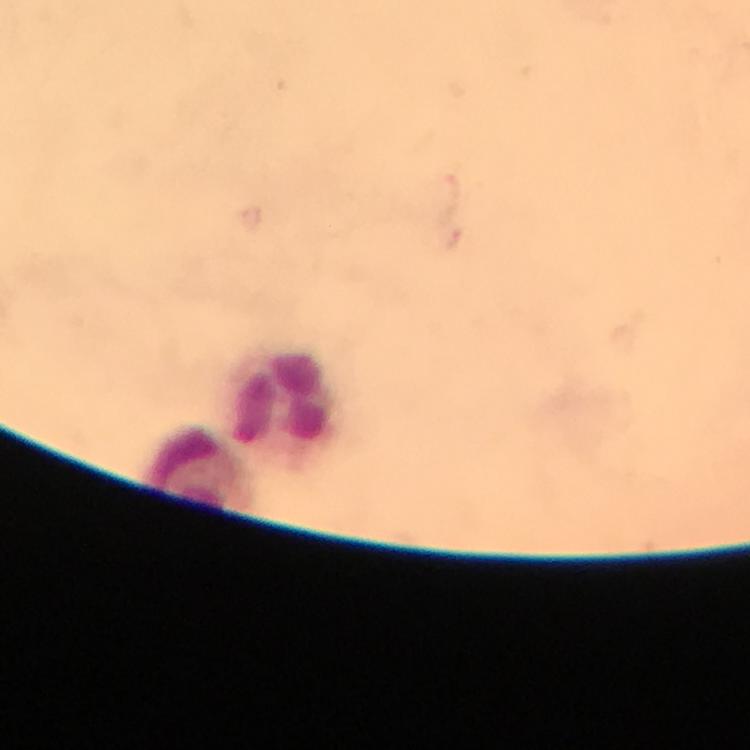
leukocyte_locations: 'approximate object centers, in pixels from the top-left corner: (x=285, y=398), (x=198, y=469)'
context: from a diagnostic examination for malaria
image_size: 750×750 pixels
plasmodium_parasites: none detected
magnification: 100x
immersion_oil: used
preparation: thick blood film
cropped_from: one field of view
stain: Giemsa
capture: smartphone camera through the microscope